Assess this cell for malaria.
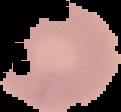

Uninfected.

The area outside the segmented cell region is set to black. From a thin blood smear. Image is 121×112 pixels.